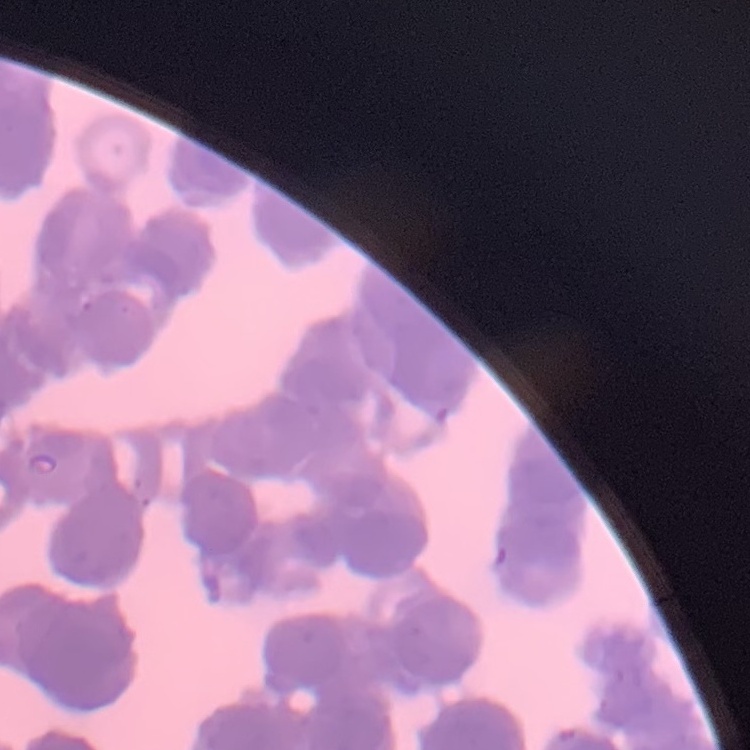
Summary:
  - Red blood cell morphology: rouleaux formation
  - Preparation: thin peripheral smear
  - Image type: one tile cut from a larger photomicrograph
  - Stain: Field's or Giemsa